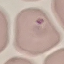

malaria status = parasitized
capture = smartphone camera at the microscope eyepiece
image type = automatically extracted cell patch, resized to 64 × 64 pixels
preparation = thin blood film
stain = Giemsa